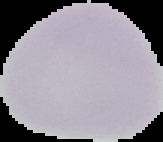

{
  "image_size": "163×142 pixels",
  "result": "no malaria parasites detected",
  "preparation": "thin blood smear",
  "image_type": "cell region segmented out of the field of view; surrounding area masked to black"
}